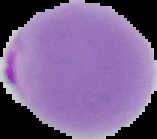
Summary:
  - Result: Plasmodium parasites detected
  - Image type: segmented cell region on a black background
  - Preparation: thin blood film
  - Image size: 157×139 pixels